Report the malaria status of this cell.
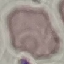
It is uninfected.

Cell patch, automatically extracted from a larger field of view and resized to 64 × 64 pixels. Acquired by smartphone through the microscope eyepiece. Thin smear of blood. Giemsa stain.